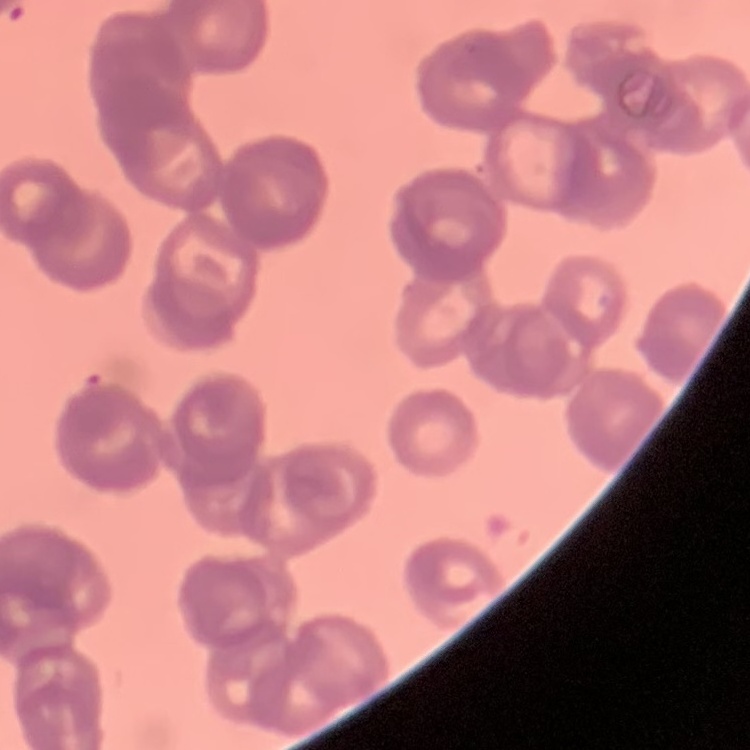
Summary:
  - Red blood cell morphology: rouleaux formation
  - Preparation: thin blood film
  - Image type: square crop of a larger photomicrograph
  - Stain: Field's or Giemsa